Outline each blood parasite and name the species.
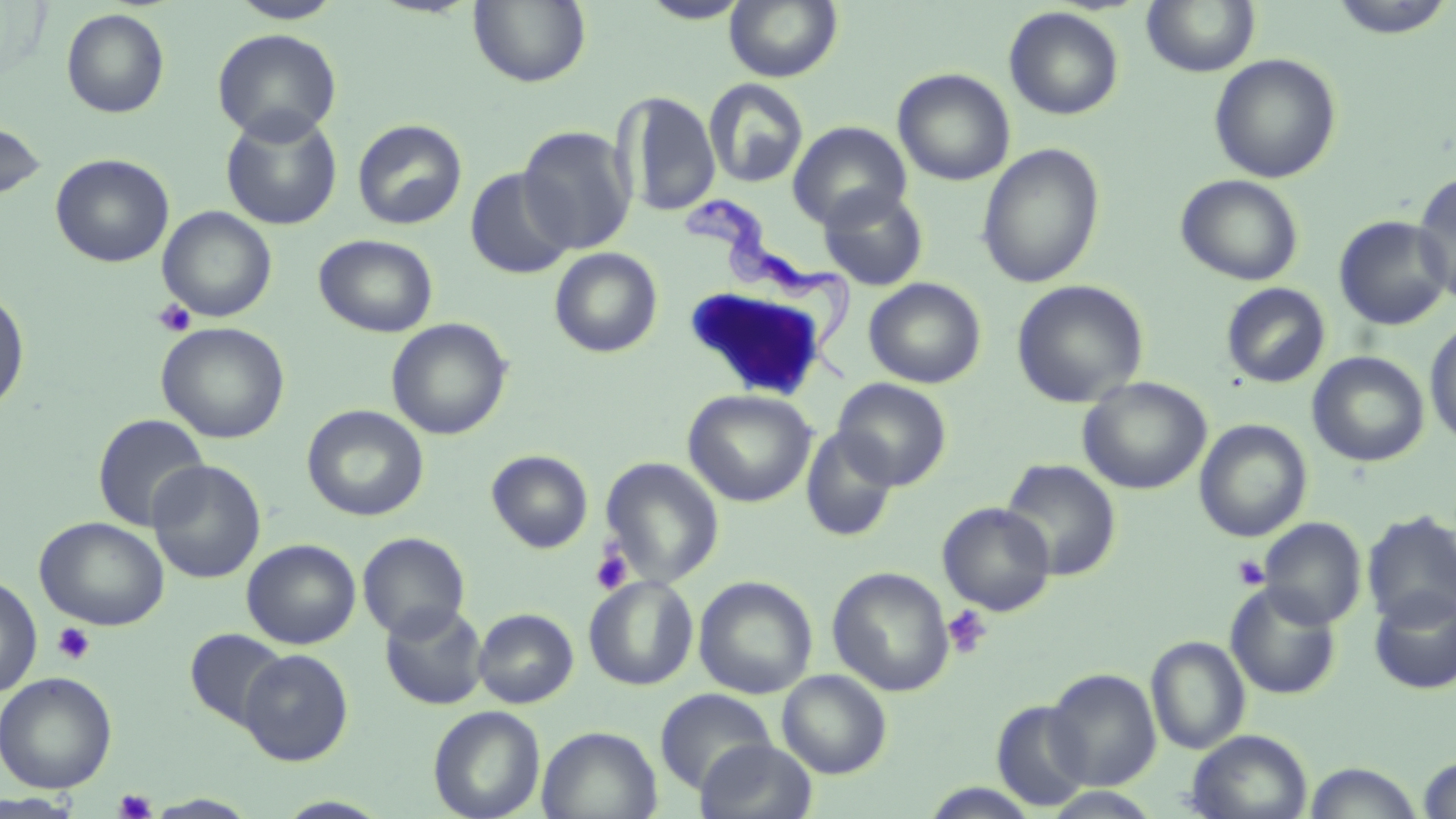
Approximate bounding boxes as (x1, y1, x2, y2) in pixels.
Trypanosoma brucei: (680, 193, 854, 385).
No Plasmodium falciparum, Plasmodium ovale, Plasmodium malariae, Plasmodium vivax, or Babesia divergens observed.

{
  "slide_level_diagnosis": "Trypanosoma brucei",
  "uninfected_red_blood_cell_locations": "approximate bounding boxes as (x1, y1, x2, y2) in pixels: (469, 0, 591, 88), (637, 0, 754, 24), (724, 0, 842, 82), (1324, 0, 1456, 40), (227, 1, 345, 24), (1141, 1, 1260, 77), (1003, 7, 1124, 120), (61, 8, 170, 118), (211, 28, 342, 144), (1209, 52, 1342, 184), (893, 68, 1016, 186), (703, 78, 809, 189), (618, 91, 721, 216), (220, 110, 343, 231), (0, 118, 47, 202), (352, 119, 467, 230), (787, 121, 911, 231), (517, 124, 638, 256), (976, 142, 1105, 288), (51, 153, 174, 268), (464, 167, 576, 279), (1412, 172, 1456, 305), (1176, 174, 1304, 286), (818, 186, 928, 291), (158, 206, 277, 322), (1334, 215, 1454, 331), (314, 234, 438, 337), (549, 247, 663, 358), (864, 278, 987, 389), (1011, 279, 1149, 408), (1221, 283, 1330, 388), (0, 288, 30, 414), (1425, 316, 1456, 449), (386, 318, 512, 440), (156, 322, 290, 443), (1308, 351, 1429, 467), (1077, 377, 1212, 495), (832, 378, 952, 490), (683, 389, 816, 507), (302, 404, 429, 522), (92, 413, 210, 531), (1194, 419, 1312, 542), (800, 427, 899, 544), (486, 449, 593, 553), (599, 457, 725, 588), (1000, 458, 1121, 581), (147, 459, 266, 584), (937, 502, 1056, 616), (1362, 510, 1456, 629), (35, 516, 169, 631), (1258, 517, 1366, 630), (358, 532, 470, 640), (242, 538, 361, 649), (827, 566, 955, 696), (0, 573, 42, 698), (583, 575, 699, 691), (693, 576, 818, 700), (1225, 583, 1342, 700), (1368, 587, 1456, 694), (380, 602, 488, 710), (473, 608, 579, 709), (185, 627, 290, 730), (1145, 635, 1250, 754), (238, 649, 353, 765), (1046, 669, 1161, 790), (777, 670, 891, 778), (0, 672, 117, 793), (654, 688, 777, 794), (993, 700, 1093, 810), (428, 705, 545, 818), (537, 725, 662, 819), (1186, 729, 1313, 819), (696, 738, 818, 819), (1417, 755, 1456, 818), (1302, 762, 1424, 819), (1042, 788, 1165, 819), (0, 791, 82, 817)",
  "preparation": "thin blood film",
  "modality": "optical microscopy",
  "stain": "May-Grünwald-Giemsa",
  "field_of_view": "one of a larger specimen",
  "image_size": "1456×819 pixels",
  "platelet_locations": "approximate bounding boxes as (x1, y1, x2, y2) in pixels: (153, 298, 196, 337), (590, 546, 634, 595), (1232, 554, 1270, 590), (943, 605, 993, 658), (52, 622, 96, 665), (114, 788, 157, 818)",
  "magnification": "1000x"
}